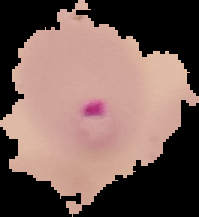

image type = segmented cell region on a black background
image size = 199×217 pixels
result = malaria parasites detected
preparation = thin blood smear